Point out each leukocyte.
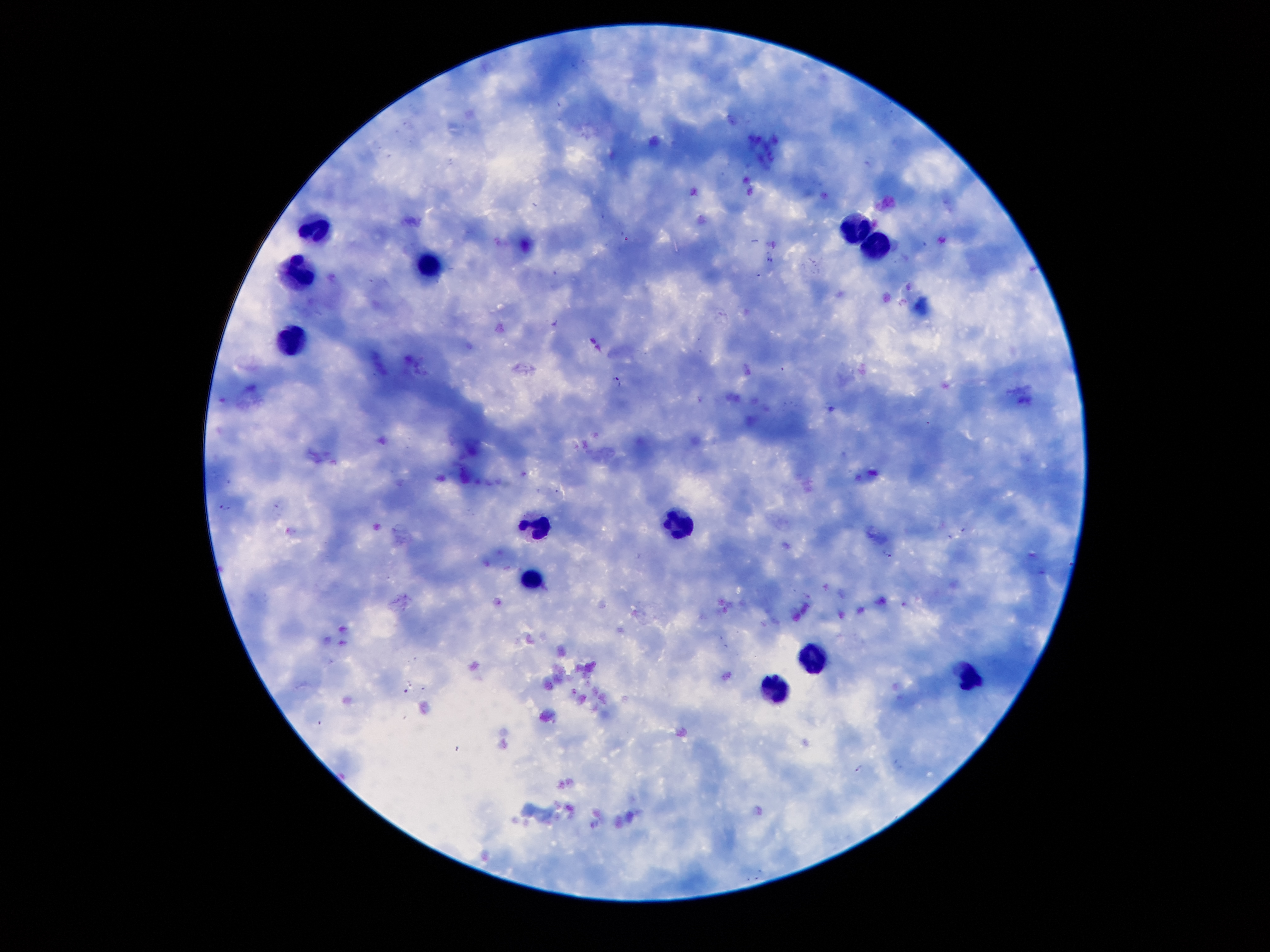
Approximate object centers, in pixels from the top-left corner.
Leukocytes: (x=314, y=225), (x=859, y=227), (x=879, y=247), (x=428, y=264), (x=292, y=269), (x=297, y=338), (x=684, y=523), (x=538, y=525), (x=532, y=579), (x=808, y=656), (x=972, y=680), (x=778, y=689).

Plasmodium parasite locations: (x=618, y=380), (x=225, y=507), (x=888, y=554), (x=859, y=768). Thick peripheral-blood smear. Patient malaria status: infected with Plasmodium falciparum. 100x magnification. Single field of view. Image is 1270×952 pixels. Giemsa stain. Smartphone photograph taken through the microscope eyepiece.